Locate every Plasmodium parasite.
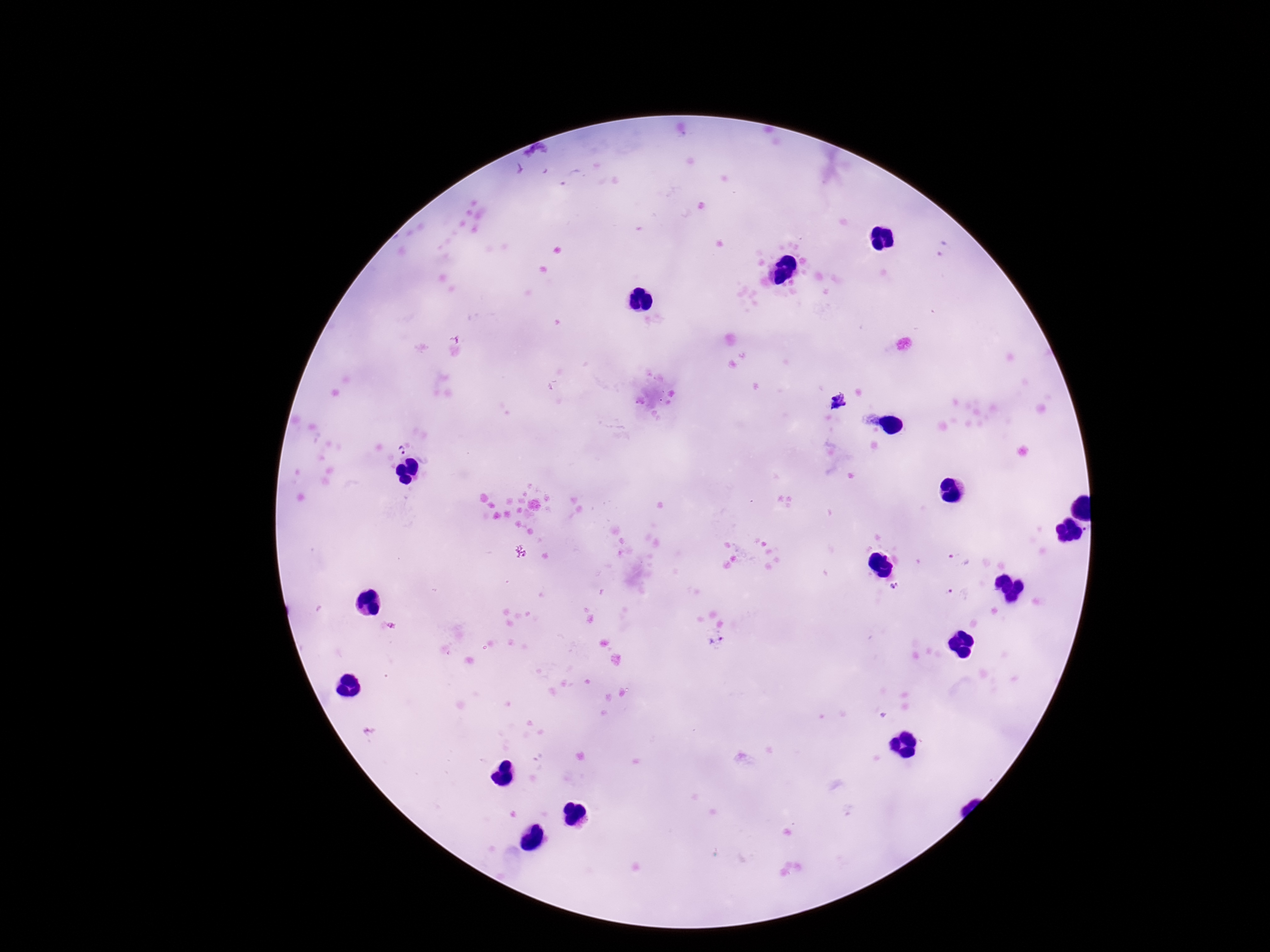

Approximate centers as [x, y] in pixels.
Plasmodium parasites: [943, 249], [839, 402], [400, 449], [1086, 527], [959, 558], [895, 586], [957, 594], [716, 640].

Image is 1270×952 pixels. Giemsa stain. 100x magnification. Patient malaria status: positive. One field from this slide. Smartphone photograph taken through the microscope eyepiece. Thick blood film.